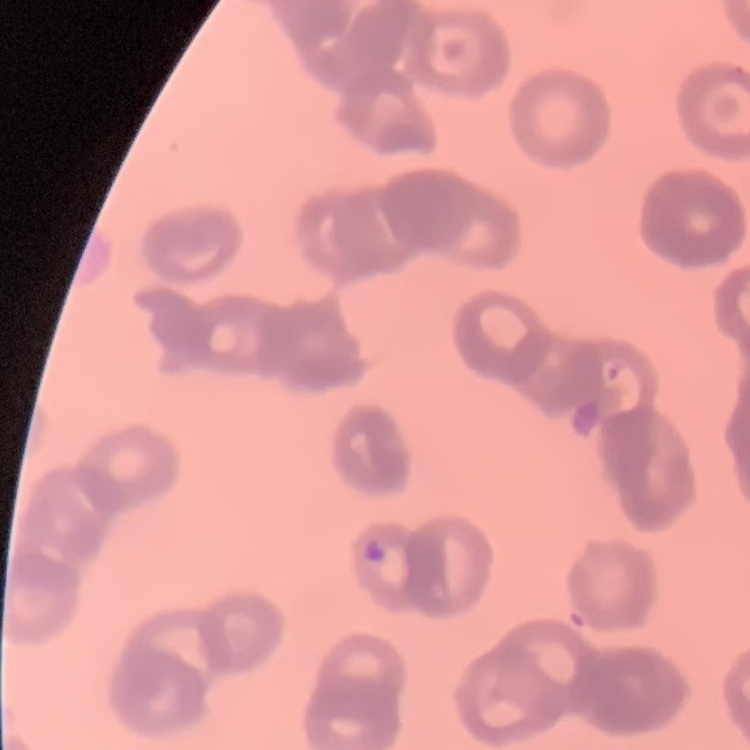

erythrocyte_morphology: rouleaux formation
stain: Field's or Giemsa
image_type: one tile cut from a larger photomicrograph
preparation: thin blood smear